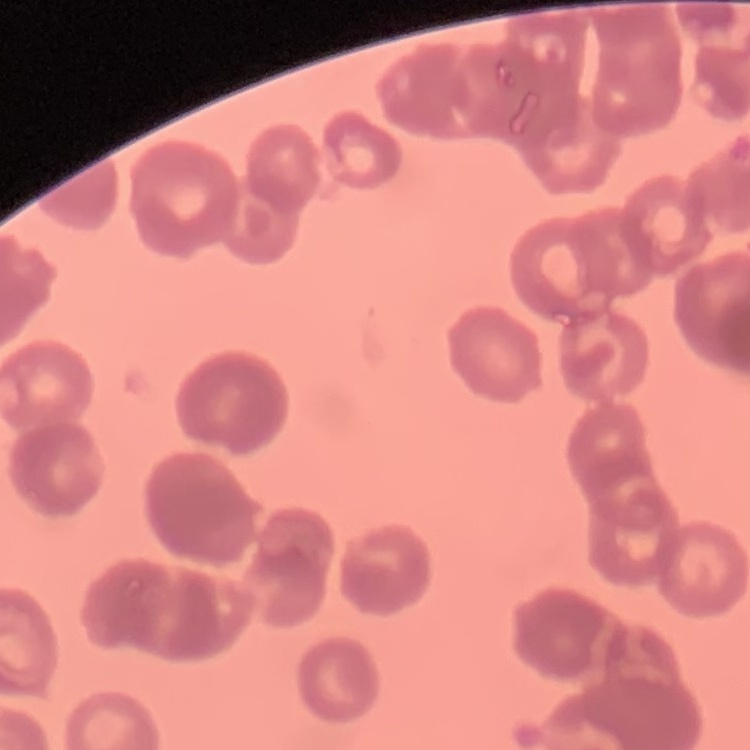
The red blood cells exhibit rouleaux formation. Stained with either Field's or Giemsa. Thin blood film. Square crop of a larger photomicrograph.